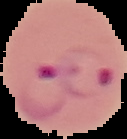

From a thin blood smear. Result: malaria parasites detected. The area outside the segmented cell region is set to black. Image is 127×139 pixels.